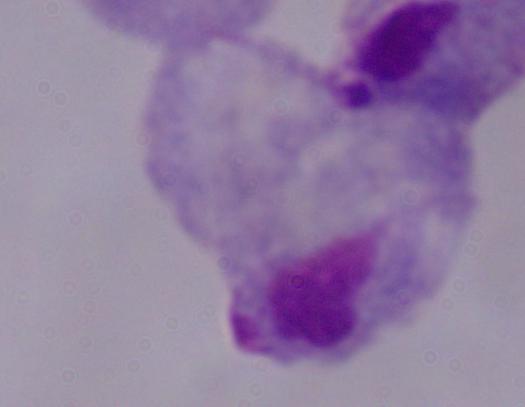

Summary:
  - Identification: trichomonad
  - Modality: micrograph
  - Magnification: 1000x